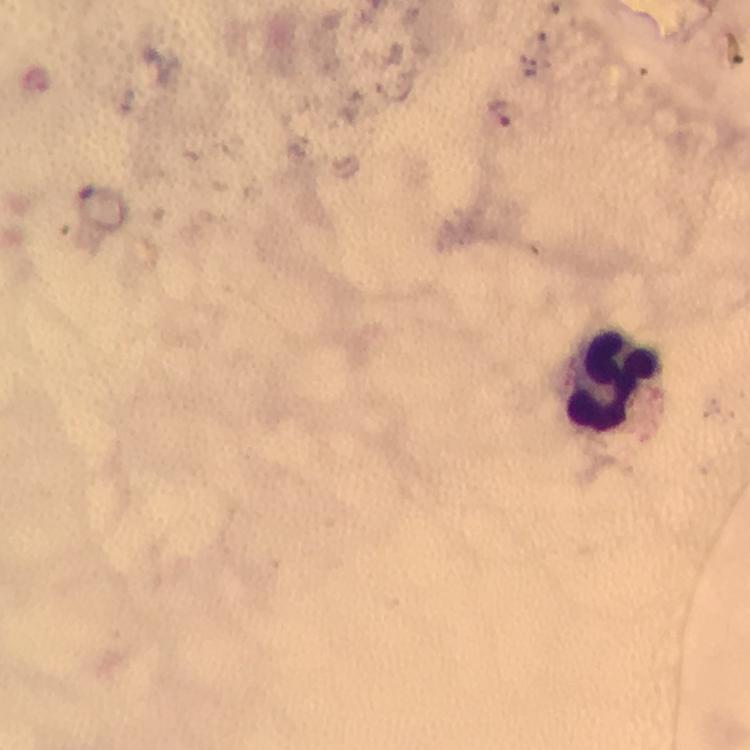
Approximate centers as [x, y] in pixels.
Summary:
  - Plasmodium parasite locations: [498, 115]
  - Leukocyte locations: [614, 387]
  - Immersion oil: applied
  - Stain: Giemsa
  - Capture: smartphone camera through the microscope
  - Context: from a diagnostic examination for malaria
  - Preparation: thick blood smear
  - Cropped from: a single field of view
  - Image size: 750×750 pixels
  - Magnification: 100x